Locate and identify every blood parasite.
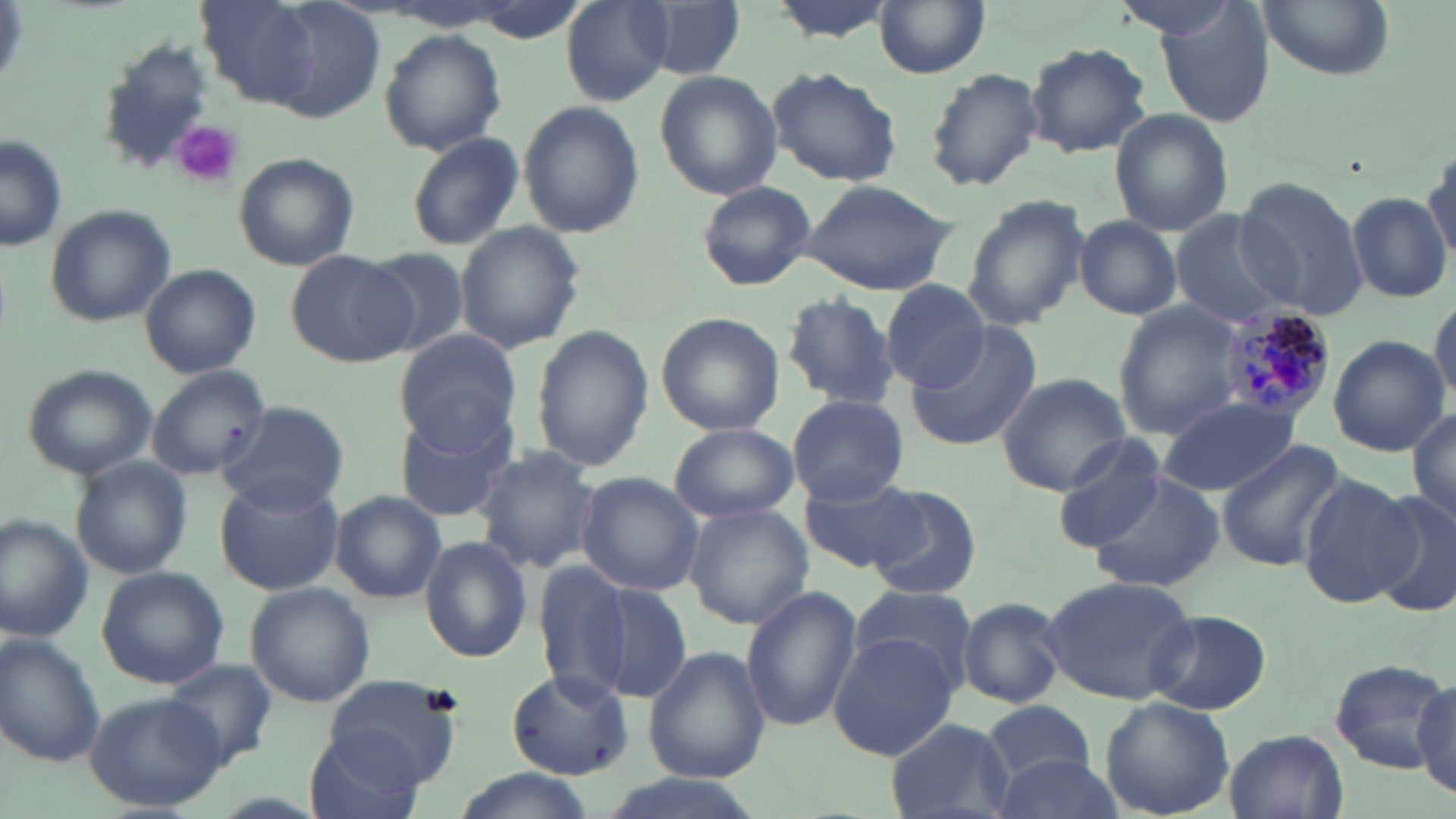

Approximate bounding boxes as (x1, y1, x2, y2) in pixels.
Plasmodium malariae-infected red blood cells: (1213, 302, 1338, 421).
No Plasmodium falciparum, Plasmodium ovale, Plasmodium vivax, Babesia divergens, or Trypanosoma brucei observed.

Summary:
  - Platelet locations: (171, 123, 244, 186)
  - Uninfected red blood cell locations: (559, 1, 674, 104), (633, 1, 744, 79), (875, 1, 991, 78), (1110, 1, 1248, 40), (1255, 2, 1394, 82), (1155, 7, 1275, 127), (379, 29, 507, 154), (99, 36, 209, 169), (1023, 41, 1153, 158), (766, 66, 902, 187), (924, 66, 1045, 194), (654, 70, 779, 200), (517, 99, 644, 237), (1110, 107, 1235, 237), (408, 133, 523, 250), (0, 136, 67, 252), (1423, 143, 1456, 267), (233, 152, 360, 271), (1234, 174, 1367, 318), (801, 177, 956, 295), (696, 179, 816, 292), (1347, 192, 1451, 304), (962, 196, 1089, 332), (45, 203, 176, 326), (1170, 213, 1290, 327), (1075, 216, 1183, 318), (454, 220, 587, 354), (362, 248, 469, 356), (286, 251, 416, 368), (141, 264, 261, 378), (881, 280, 988, 390), (780, 292, 902, 410), (1428, 294, 1456, 411), (1114, 303, 1245, 437), (656, 312, 785, 436), (905, 322, 1042, 452), (531, 325, 653, 474), (394, 329, 520, 451), (1328, 334, 1449, 457), (22, 363, 157, 478), (148, 365, 272, 482), (996, 372, 1131, 496), (786, 394, 910, 505), (1154, 396, 1304, 496), (217, 400, 348, 512), (392, 406, 519, 524), (1407, 407, 1456, 526), (668, 423, 799, 524), (1051, 438, 1168, 551), (1217, 441, 1349, 572), (471, 445, 598, 573), (71, 458, 192, 579), (1088, 470, 1229, 592), (575, 472, 704, 597), (215, 473, 347, 595), (1297, 475, 1423, 608), (801, 477, 925, 575), (862, 484, 983, 602), (1369, 489, 1456, 617), (330, 490, 444, 603), (682, 502, 813, 631), (0, 515, 96, 641), (418, 535, 534, 663), (537, 562, 631, 695), (96, 568, 228, 688), (1042, 574, 1198, 705), (245, 582, 374, 708), (592, 583, 692, 702), (847, 584, 980, 691), (739, 586, 861, 733), (956, 597, 1067, 710), (1144, 610, 1273, 717), (0, 635, 105, 766), (827, 635, 960, 760), (643, 645, 770, 785), (159, 657, 280, 766), (1329, 657, 1453, 774), (508, 669, 633, 780), (323, 674, 465, 786), (1413, 675, 1456, 800), (84, 688, 228, 812), (982, 697, 1096, 784), (1098, 697, 1236, 818), (885, 716, 1014, 819), (305, 728, 426, 819), (1223, 729, 1347, 819), (989, 750, 1128, 819), (449, 767, 596, 819), (585, 772, 766, 819)
  - Slide-level diagnosis: Plasmodium malariae
  - Modality: optical microscopy
  - Field of view: one of a larger specimen
  - Preparation: thin blood smear
  - Stain: May-Grünwald-Giemsa
  - Magnification: 1000x
  - Image size: 1456×819 pixels